Report the malaria status of this cell.
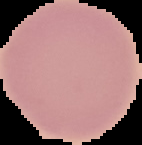

It is uninfected.

image type = segmented cell region on a black background
image size = 142×145 pixels
preparation = thin blood film